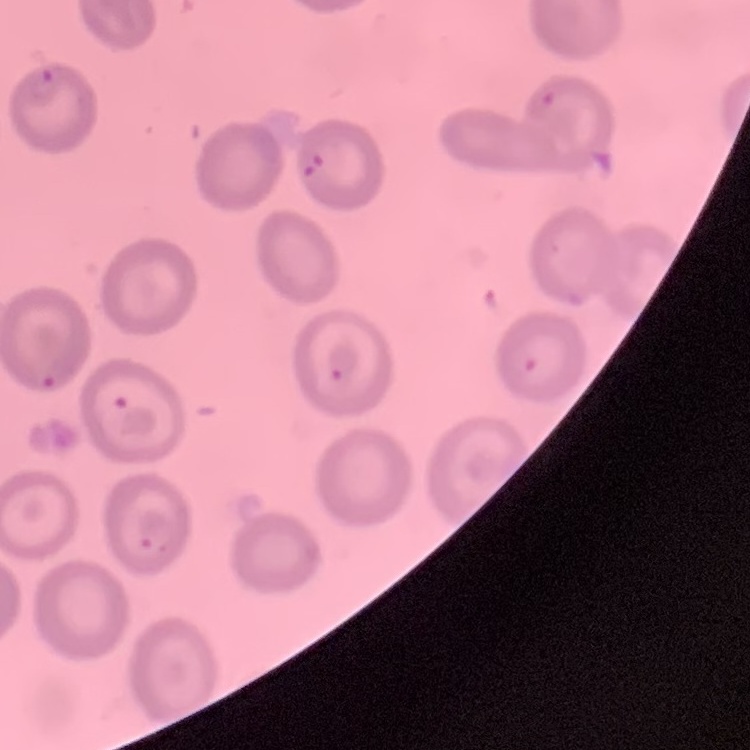

The red blood cells show no rouleaux formation. Square crop of a larger photomicrograph. Thin blood smear. Field's or Giemsa stain.